Classify this cell by malaria status.
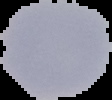

Uninfected.

From a thin blood smear. The area outside the segmented cell region is set to black. Image is 112×100 pixels.